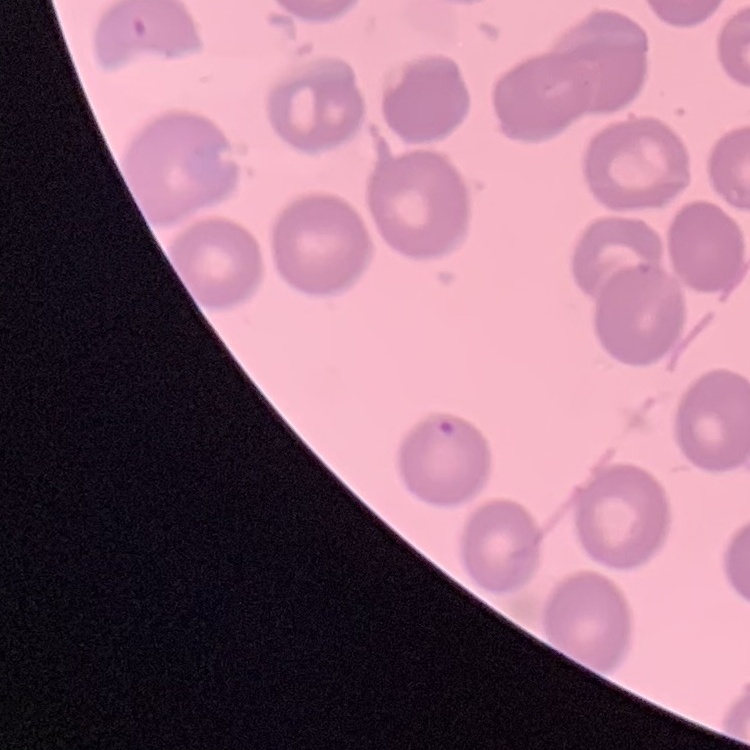

Summary:
  - Erythrocyte morphology: no rouleaux formation
  - Preparation: thin peripheral smear
  - Stain: Field's or Giemsa
  - Image type: one tile cut from a larger photomicrograph